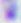

identification = Toxoplasma gondii
magnification = 400x
modality = micrograph